Point out each Plasmodium parasite.
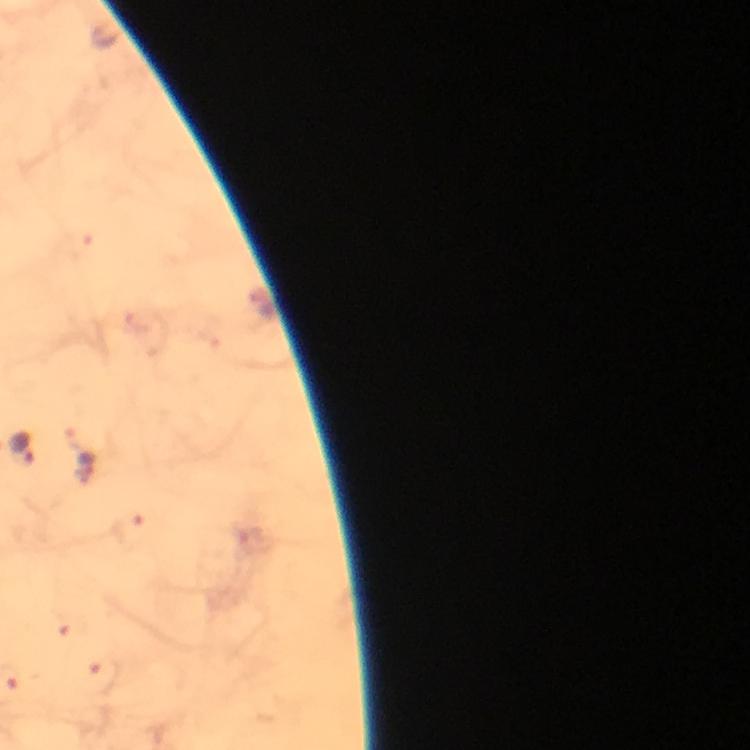

Approximate centers as [x, y] in pixels.
Plasmodium parasites: [22, 450], [87, 469].

A crop from one field of view. Image is 750×750 pixels. Thick blood film. From a malaria diagnostic workup. Giemsa-stained preparation. At 100x magnification. Immersion oil applied. Smartphone photograph taken through a microscope.